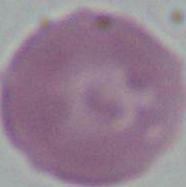

modality = micrograph
identification = red blood cell
magnification = 1000x